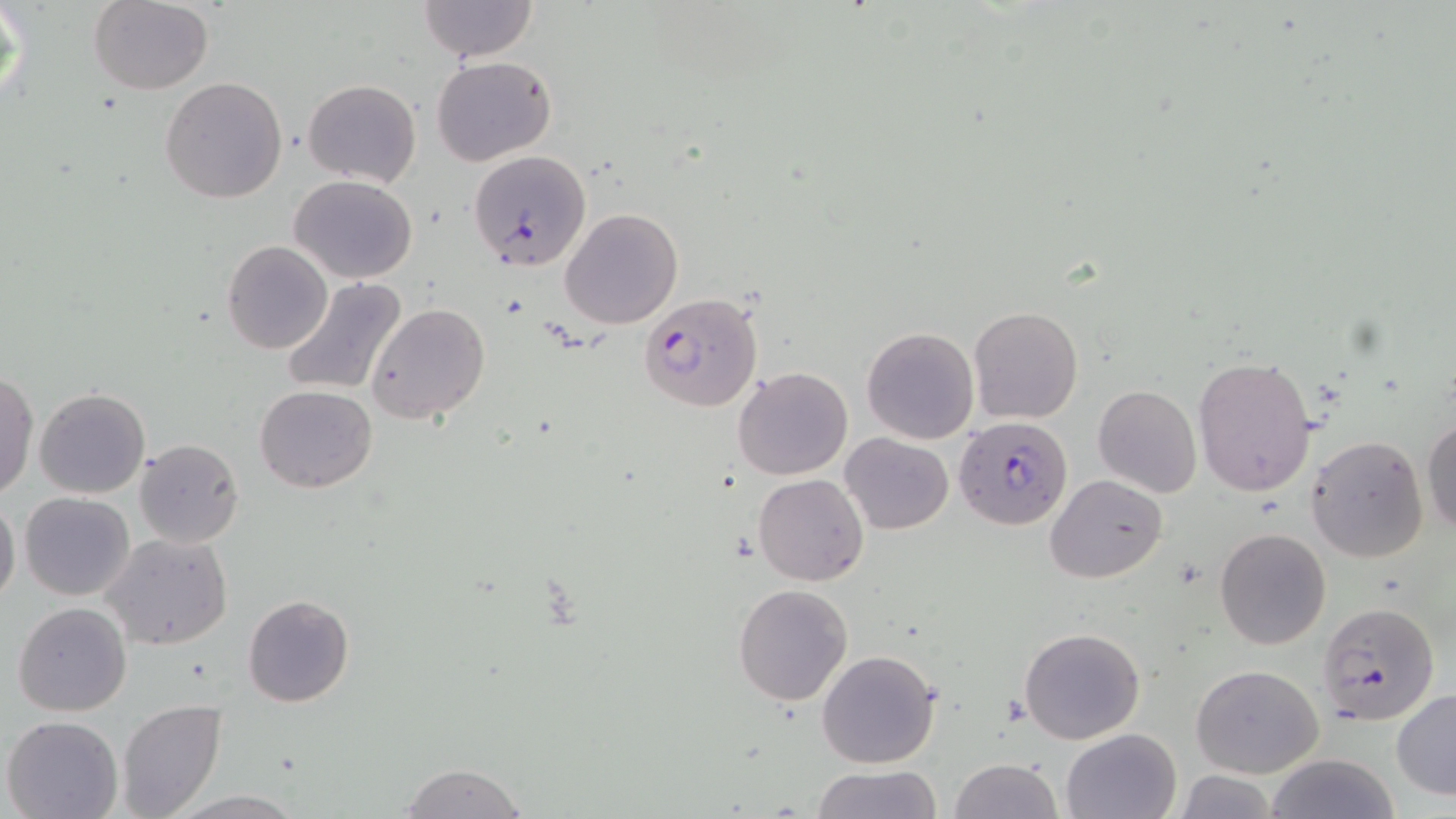
Approximate bounding boxes as [x1, y1, x2, y2] in pixels. Plasmodium falciparum-infected red blood cell locations: [468, 150, 592, 272], [640, 292, 763, 410], [953, 416, 1073, 530], [1317, 600, 1439, 724]. Uninfected red blood cell locations: [416, 0, 540, 62], [1, 1, 28, 117], [89, 2, 214, 95], [433, 56, 556, 168], [160, 77, 287, 204], [301, 78, 421, 186], [289, 175, 418, 283], [561, 208, 683, 330], [222, 241, 331, 354], [279, 277, 408, 396], [366, 302, 490, 424], [968, 307, 1083, 424], [861, 326, 979, 444], [1192, 357, 1317, 496], [733, 366, 853, 480], [0, 370, 38, 499], [255, 384, 378, 493], [1092, 385, 1202, 498], [34, 387, 151, 498], [1423, 417, 1456, 534], [840, 432, 952, 534], [1306, 435, 1429, 564], [135, 438, 243, 547], [752, 472, 870, 585], [1045, 473, 1165, 584], [20, 492, 133, 602], [0, 496, 21, 608], [1215, 527, 1332, 649], [101, 532, 233, 651], [733, 583, 853, 705], [242, 594, 354, 707], [12, 603, 131, 717], [1019, 627, 1146, 744], [816, 648, 941, 769], [1191, 663, 1324, 778], [1391, 688, 1456, 799], [117, 700, 227, 819], [2, 715, 124, 818], [1061, 728, 1182, 818], [1266, 752, 1400, 819], [949, 758, 1062, 818], [399, 762, 529, 819], [809, 764, 942, 819], [1171, 772, 1282, 818], [170, 790, 305, 818]. Slide-level diagnosis: Plasmodium falciparum. May-Grünwald-Giemsa stain. 1000x magnification. Thin blood film. Single field of view. Image is 1456×819 pixels. Light microscopy.